Assess this cell for malaria.
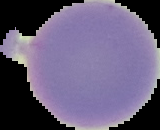
It is uninfected.

Summary:
  - Image type: segmented cell region on a black background
  - Image size: 160×130 pixels
  - Preparation: thin blood smear